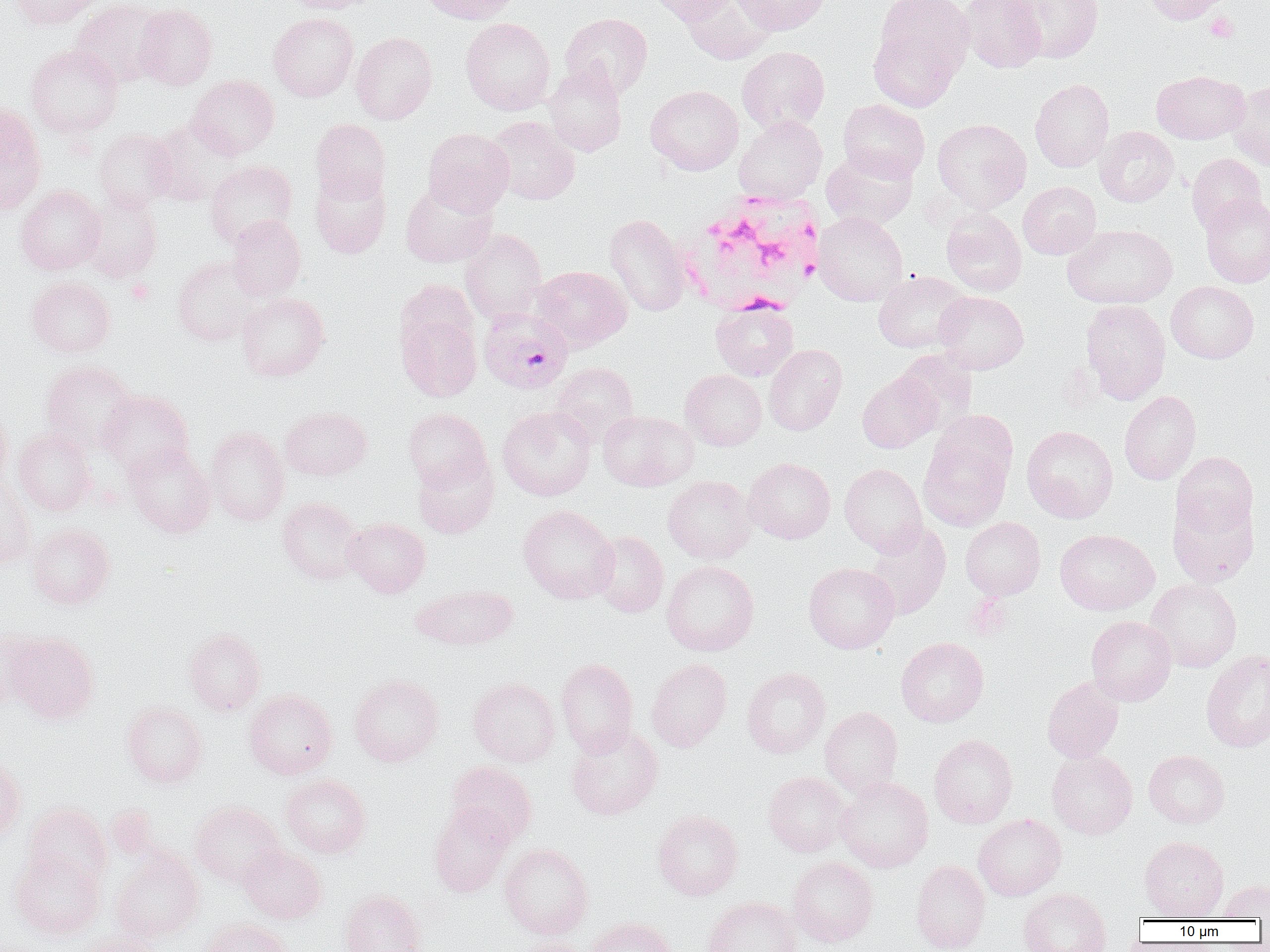

slide-level diagnosis = Plasmodium falciparum
magnification = 1000x
modality = optical microscopy
platelet locations = approximate bounding boxes as named x1/y1/x2/y2 corners in pixels: (x1=1205, y1=12, x2=1238, y2=42), (x1=127, y1=279, x2=155, y2=304)
field of view = one of a larger specimen
uninfected red blood cell locations = approximate bounding boxes as named x1/y1/x2/y2 corners in pixels: (x1=8, y1=0, x2=103, y2=29), (x1=280, y1=0, x2=380, y2=13), (x1=419, y1=0, x2=520, y2=24), (x1=645, y1=0, x2=737, y2=24), (x1=682, y1=0, x2=777, y2=65), (x1=733, y1=0, x2=831, y2=35), (x1=874, y1=0, x2=974, y2=77), (x1=960, y1=0, x2=1046, y2=73), (x1=1006, y1=0, x2=1103, y2=63), (x1=1142, y1=0, x2=1233, y2=25), (x1=70, y1=1, x2=165, y2=87), (x1=134, y1=5, x2=217, y2=90), (x1=268, y1=12, x2=358, y2=101), (x1=560, y1=13, x2=653, y2=98), (x1=460, y1=17, x2=556, y2=115), (x1=869, y1=27, x2=961, y2=112), (x1=351, y1=32, x2=437, y2=124), (x1=26, y1=44, x2=123, y2=137), (x1=737, y1=46, x2=830, y2=132), (x1=543, y1=64, x2=628, y2=156), (x1=1151, y1=70, x2=1249, y2=144), (x1=187, y1=75, x2=279, y2=159), (x1=1030, y1=78, x2=1114, y2=172), (x1=1227, y1=80, x2=1270, y2=170), (x1=645, y1=85, x2=743, y2=175), (x1=838, y1=99, x2=930, y2=182), (x1=0, y1=102, x2=46, y2=215), (x1=734, y1=115, x2=827, y2=204), (x1=485, y1=116, x2=580, y2=205), (x1=148, y1=117, x2=243, y2=207), (x1=310, y1=119, x2=390, y2=203), (x1=932, y1=119, x2=1031, y2=212), (x1=1095, y1=126, x2=1178, y2=207), (x1=422, y1=128, x2=514, y2=216), (x1=94, y1=129, x2=177, y2=211), (x1=821, y1=149, x2=918, y2=230), (x1=1186, y1=153, x2=1266, y2=234), (x1=205, y1=160, x2=297, y2=248), (x1=310, y1=168, x2=391, y2=258), (x1=401, y1=181, x2=497, y2=267), (x1=1018, y1=182, x2=1101, y2=259), (x1=15, y1=185, x2=105, y2=274), (x1=82, y1=192, x2=162, y2=283), (x1=1200, y1=194, x2=1270, y2=287), (x1=941, y1=208, x2=1026, y2=296), (x1=813, y1=212, x2=907, y2=306), (x1=605, y1=214, x2=690, y2=316), (x1=225, y1=215, x2=305, y2=301), (x1=1063, y1=223, x2=1177, y2=309), (x1=461, y1=229, x2=547, y2=322), (x1=173, y1=256, x2=263, y2=346), (x1=532, y1=265, x2=631, y2=351), (x1=873, y1=271, x2=970, y2=353), (x1=27, y1=277, x2=115, y2=357), (x1=1166, y1=281, x2=1258, y2=363), (x1=934, y1=291, x2=1029, y2=373), (x1=237, y1=293, x2=329, y2=381), (x1=395, y1=299, x2=482, y2=402), (x1=1081, y1=299, x2=1171, y2=404), (x1=711, y1=301, x2=798, y2=381), (x1=764, y1=344, x2=847, y2=435), (x1=895, y1=350, x2=977, y2=435), (x1=40, y1=361, x2=137, y2=452), (x1=551, y1=362, x2=638, y2=444), (x1=680, y1=369, x2=766, y2=450), (x1=857, y1=371, x2=941, y2=453), (x1=98, y1=390, x2=193, y2=476), (x1=1119, y1=390, x2=1201, y2=485), (x1=0, y1=405, x2=12, y2=495), (x1=497, y1=405, x2=596, y2=500), (x1=280, y1=406, x2=371, y2=480), (x1=403, y1=408, x2=490, y2=490), (x1=932, y1=409, x2=1018, y2=486), (x1=598, y1=411, x2=697, y2=491), (x1=1021, y1=425, x2=1118, y2=523), (x1=205, y1=426, x2=289, y2=525), (x1=13, y1=427, x2=97, y2=515), (x1=919, y1=433, x2=1012, y2=531), (x1=124, y1=443, x2=215, y2=537), (x1=413, y1=451, x2=498, y2=538), (x1=1171, y1=451, x2=1259, y2=539), (x1=743, y1=458, x2=835, y2=543), (x1=839, y1=463, x2=927, y2=555), (x1=662, y1=475, x2=756, y2=564), (x1=0, y1=482, x2=34, y2=569), (x1=1168, y1=494, x2=1259, y2=587), (x1=277, y1=496, x2=365, y2=585), (x1=518, y1=505, x2=619, y2=603), (x1=960, y1=517, x2=1045, y2=600), (x1=344, y1=518, x2=429, y2=597), (x1=866, y1=522, x2=951, y2=619), (x1=28, y1=523, x2=115, y2=608), (x1=1055, y1=529, x2=1159, y2=615), (x1=589, y1=530, x2=669, y2=617), (x1=662, y1=561, x2=759, y2=656), (x1=803, y1=562, x2=899, y2=653), (x1=1146, y1=579, x2=1242, y2=672), (x1=413, y1=584, x2=518, y2=650), (x1=1086, y1=615, x2=1176, y2=705), (x1=0, y1=627, x2=39, y2=710), (x1=185, y1=628, x2=265, y2=715), (x1=6, y1=633, x2=99, y2=723), (x1=896, y1=637, x2=989, y2=727), (x1=1201, y1=650, x2=1270, y2=752), (x1=556, y1=658, x2=638, y2=756), (x1=646, y1=658, x2=732, y2=751), (x1=742, y1=667, x2=830, y2=758), (x1=349, y1=674, x2=444, y2=767), (x1=468, y1=677, x2=560, y2=766), (x1=1041, y1=677, x2=1124, y2=763), (x1=244, y1=689, x2=337, y2=779), (x1=122, y1=701, x2=208, y2=787), (x1=820, y1=706, x2=903, y2=797), (x1=565, y1=725, x2=663, y2=820), (x1=928, y1=733, x2=1018, y2=828), (x1=1143, y1=749, x2=1230, y2=828), (x1=1047, y1=750, x2=1137, y2=839), (x1=0, y1=756, x2=26, y2=842), (x1=446, y1=760, x2=537, y2=845), (x1=763, y1=771, x2=851, y2=857), (x1=281, y1=773, x2=370, y2=858), (x1=835, y1=776, x2=933, y2=872), (x1=191, y1=801, x2=284, y2=886), (x1=23, y1=803, x2=111, y2=890), (x1=429, y1=803, x2=513, y2=896), (x1=652, y1=809, x2=743, y2=900), (x1=973, y1=814, x2=1066, y2=901), (x1=1139, y1=835, x2=1228, y2=919), (x1=499, y1=843, x2=593, y2=939), (x1=239, y1=845, x2=327, y2=923), (x1=10, y1=849, x2=104, y2=939), (x1=111, y1=849, x2=203, y2=942), (x1=788, y1=857, x2=878, y2=947), (x1=910, y1=860, x2=990, y2=952), (x1=1218, y1=880, x2=1270, y2=919), (x1=1018, y1=887, x2=1111, y2=952), (x1=340, y1=888, x2=425, y2=952), (x1=703, y1=897, x2=800, y2=952), (x1=587, y1=917, x2=677, y2=952), (x1=201, y1=918, x2=293, y2=952), (x1=72, y1=931, x2=164, y2=952), (x1=508, y1=937, x2=590, y2=952)
white blood cell locations = approximate bounding boxes as named x1/y1/x2/y2 corners in pixels: (x1=678, y1=191, x2=824, y2=315)
Plasmodium falciparum-infected red blood cell locations = approximate bounding boxes as named x1/y1/x2/y2 corners in pixels: (x1=478, y1=306, x2=573, y2=394)
preparation = thin blood film
image size = 1270×952 pixels